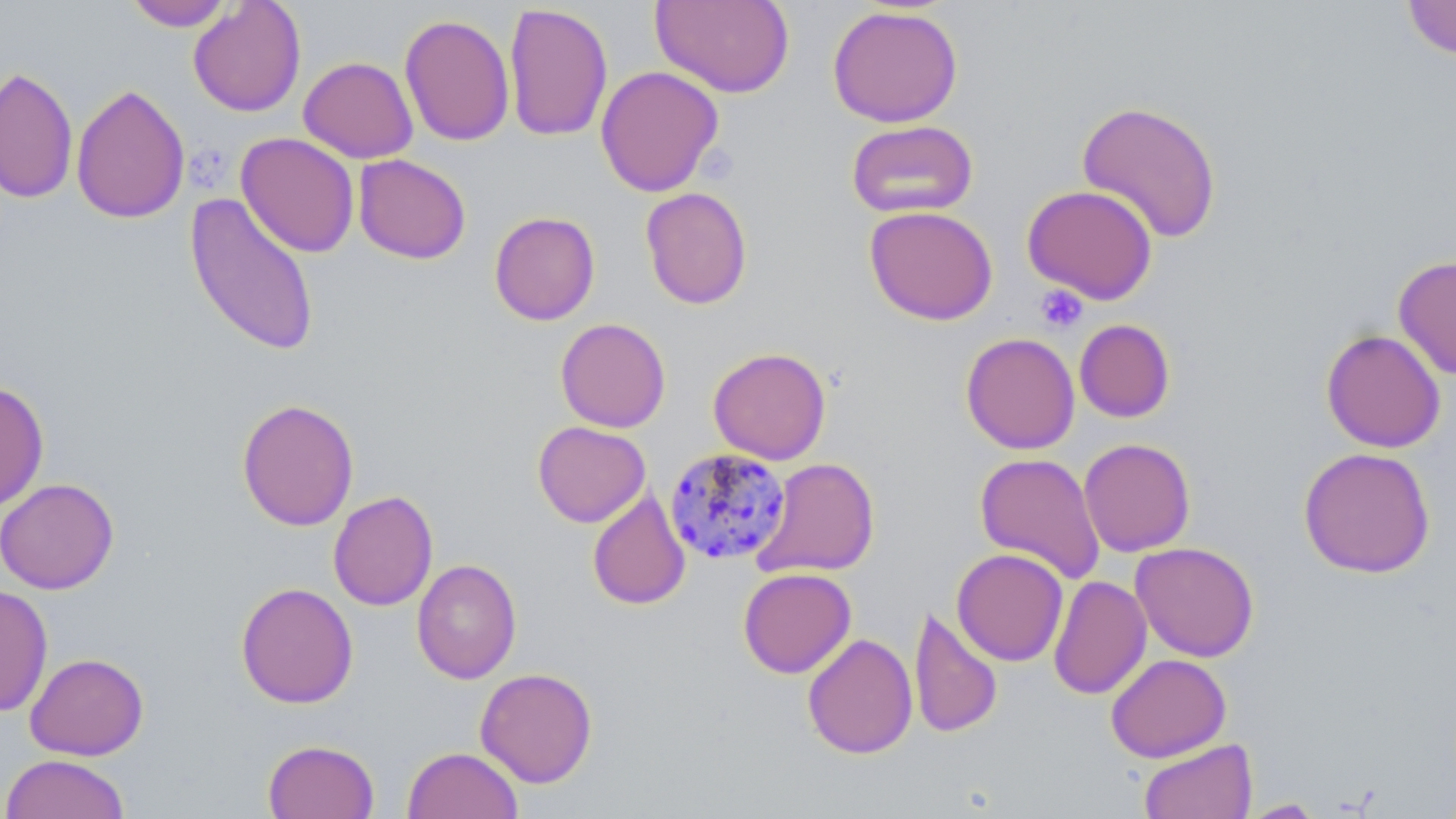
Approximate bounding boxes as (x1, y1, x2, y2) in pixels. Uninfected red blood cell locations: (650, 0, 795, 98), (1402, 0, 1456, 60), (124, 1, 236, 31), (188, 1, 306, 117), (503, 3, 613, 142), (827, 5, 964, 128), (399, 13, 515, 146), (298, 56, 418, 163), (595, 65, 724, 197), (0, 66, 78, 204), (71, 83, 190, 224), (1076, 99, 1223, 244), (846, 119, 979, 219), (236, 132, 360, 258), (353, 154, 471, 264), (1021, 184, 1158, 304), (640, 187, 752, 309), (183, 191, 322, 359), (864, 205, 998, 325), (489, 211, 601, 325), (1392, 254, 1456, 380), (555, 317, 671, 433), (1074, 318, 1175, 423), (1320, 329, 1446, 453), (961, 332, 1080, 454), (707, 346, 832, 465), (0, 379, 49, 512), (236, 398, 360, 532), (532, 421, 651, 527), (1078, 438, 1196, 557), (1298, 446, 1436, 579), (974, 452, 1106, 583), (753, 457, 881, 579), (0, 478, 119, 595), (587, 488, 691, 610), (328, 490, 438, 611), (1130, 542, 1260, 662), (952, 548, 1068, 666), (412, 559, 522, 684), (738, 567, 856, 678), (1048, 576, 1152, 700), (235, 582, 359, 709), (0, 584, 53, 717), (909, 606, 1003, 740), (802, 632, 918, 760), (25, 652, 149, 760), (1106, 653, 1231, 762), (475, 667, 598, 788), (1139, 738, 1257, 819), (262, 739, 379, 819), (402, 746, 523, 819), (1, 753, 132, 819), (1239, 798, 1325, 817). Platelet locations: (1035, 285, 1088, 333). Plasmodium malariae-infected red blood cell locations: (665, 447, 792, 566). Slide-level diagnosis: Plasmodium malariae. Image is 1456×819 pixels. May-Grünwald-Giemsa stain. Thin blood film. Single field of view. Optical microscopy. Captured at 1000x magnification.